Locate and identify every blood parasite.
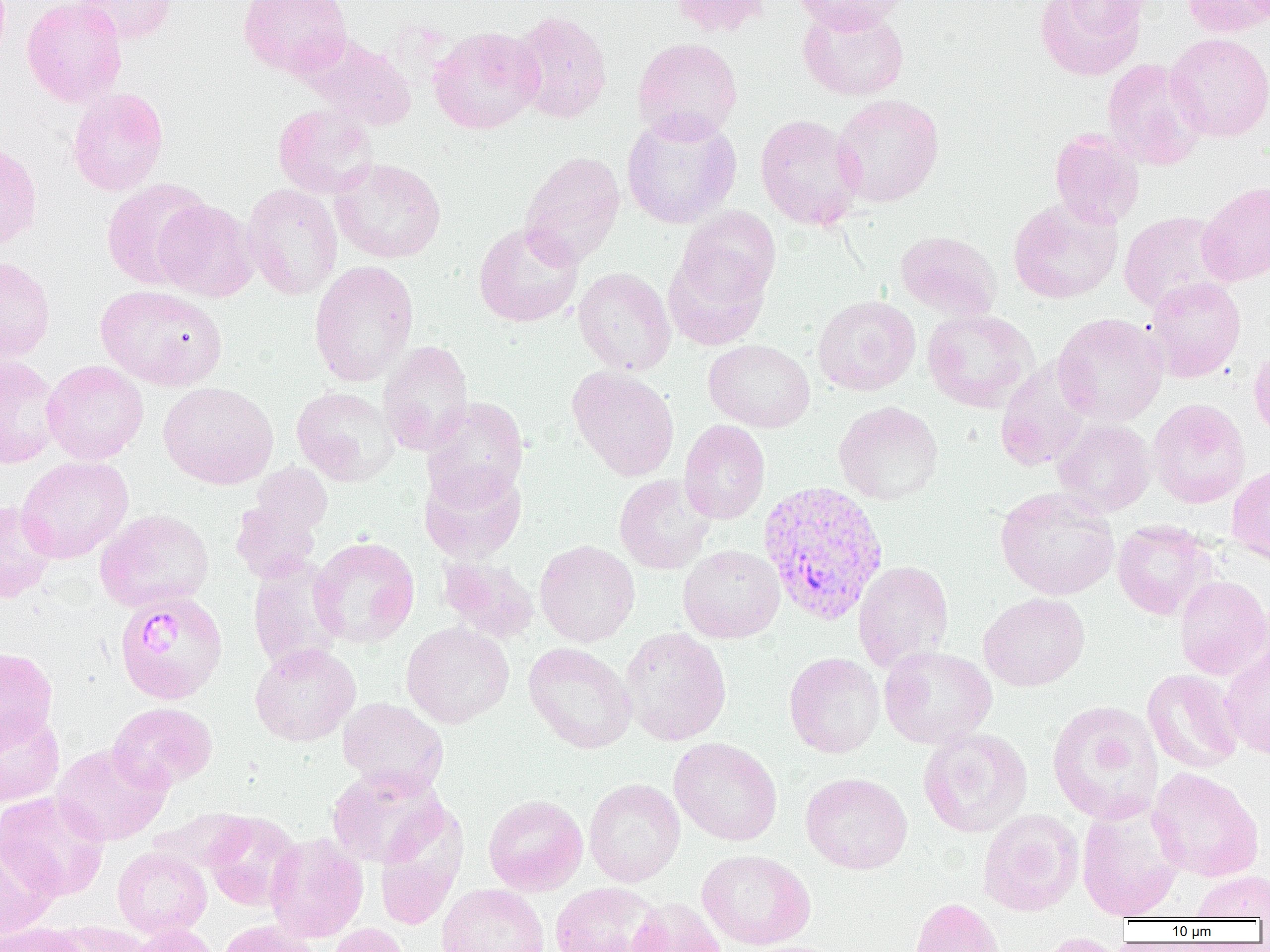
Approximate bounding boxes as (x1, y1, x2, y2) in pixels.
Plasmodium vivax-infected red blood cells: (757, 480, 888, 625), (114, 591, 228, 705).
No Plasmodium falciparum, Plasmodium ovale, Plasmodium malariae, Babesia divergens, or Trypanosoma brucei observed.

slide-level diagnosis = Plasmodium vivax
field of view = single
modality = optical microscopy
preparation = thin blood film
platelet locations = approximate bounding boxes as (x1, y1, x2, y2) in pixels: (142, 615, 182, 658)
magnification = 1000x
uninfected red blood cell locations = approximate bounding boxes as (x1, y1, x2, y2) in pixels: (22, 0, 126, 107), (73, 0, 177, 44), (239, 0, 353, 78), (670, 0, 772, 37), (792, 0, 908, 34), (1035, 0, 1146, 80), (1054, 0, 1153, 33), (1181, 0, 1269, 38), (797, 4, 909, 101), (511, 10, 613, 124), (428, 26, 545, 134), (1164, 32, 1270, 142), (300, 34, 417, 130), (632, 37, 743, 142), (1102, 59, 1207, 170), (67, 87, 169, 196), (831, 94, 944, 207), (273, 104, 378, 200), (621, 111, 742, 229), (755, 114, 864, 231), (1049, 129, 1144, 230), (0, 140, 42, 252), (520, 151, 625, 268), (330, 159, 446, 264), (102, 177, 214, 290), (1197, 181, 1270, 286), (242, 183, 343, 300), (1008, 198, 1122, 304), (154, 199, 259, 302), (674, 207, 780, 309), (1118, 211, 1235, 313), (473, 222, 584, 327), (894, 231, 1002, 321), (663, 246, 773, 351), (0, 256, 55, 362), (309, 259, 419, 386), (573, 267, 676, 376), (1144, 277, 1246, 382), (95, 284, 227, 391), (813, 295, 921, 395), (922, 309, 1038, 412), (1052, 313, 1168, 426), (378, 340, 474, 456), (704, 340, 815, 432), (1249, 345, 1270, 442), (0, 355, 62, 469), (42, 359, 148, 465), (995, 359, 1094, 472), (567, 366, 680, 481), (158, 382, 278, 489), (291, 385, 400, 486), (422, 396, 529, 506), (1147, 398, 1250, 508), (834, 401, 943, 505), (1052, 418, 1155, 516), (679, 419, 770, 524), (15, 456, 134, 563), (419, 462, 527, 563), (1227, 464, 1270, 565), (230, 469, 332, 585), (614, 475, 715, 575), (995, 487, 1120, 601), (0, 501, 56, 603), (95, 509, 215, 612), (1112, 521, 1213, 620), (309, 536, 419, 648), (534, 539, 640, 647), (678, 544, 784, 643), (438, 554, 540, 644), (247, 556, 346, 674), (853, 560, 953, 673), (1174, 575, 1270, 680), (978, 592, 1090, 691), (401, 621, 514, 728), (619, 627, 732, 746), (523, 641, 637, 754), (1220, 642, 1270, 759), (250, 643, 361, 746), (879, 646, 997, 749), (0, 647, 57, 750), (784, 652, 885, 758), (1142, 668, 1244, 774), (337, 698, 449, 796), (1047, 699, 1164, 824), (108, 702, 217, 792), (0, 710, 65, 807), (0, 710, 73, 901), (918, 727, 1032, 838), (669, 737, 782, 846), (52, 742, 172, 846), (326, 766, 447, 867), (1148, 767, 1264, 882), (800, 772, 913, 874), (584, 778, 685, 887), (1, 792, 110, 900), (483, 794, 588, 895), (1076, 802, 1186, 920), (149, 807, 254, 875), (977, 809, 1084, 916), (204, 812, 303, 911), (264, 833, 368, 944), (0, 835, 60, 939), (112, 847, 212, 938), (696, 849, 816, 950), (1190, 871, 1269, 920), (549, 882, 666, 952), (436, 883, 549, 952), (909, 897, 1007, 952), (628, 898, 727, 952), (216, 921, 321, 952), (59, 922, 152, 952), (1, 923, 88, 952), (327, 923, 413, 952), (127, 924, 222, 952), (1032, 932, 1129, 952)
image size = 1270×952 pixels